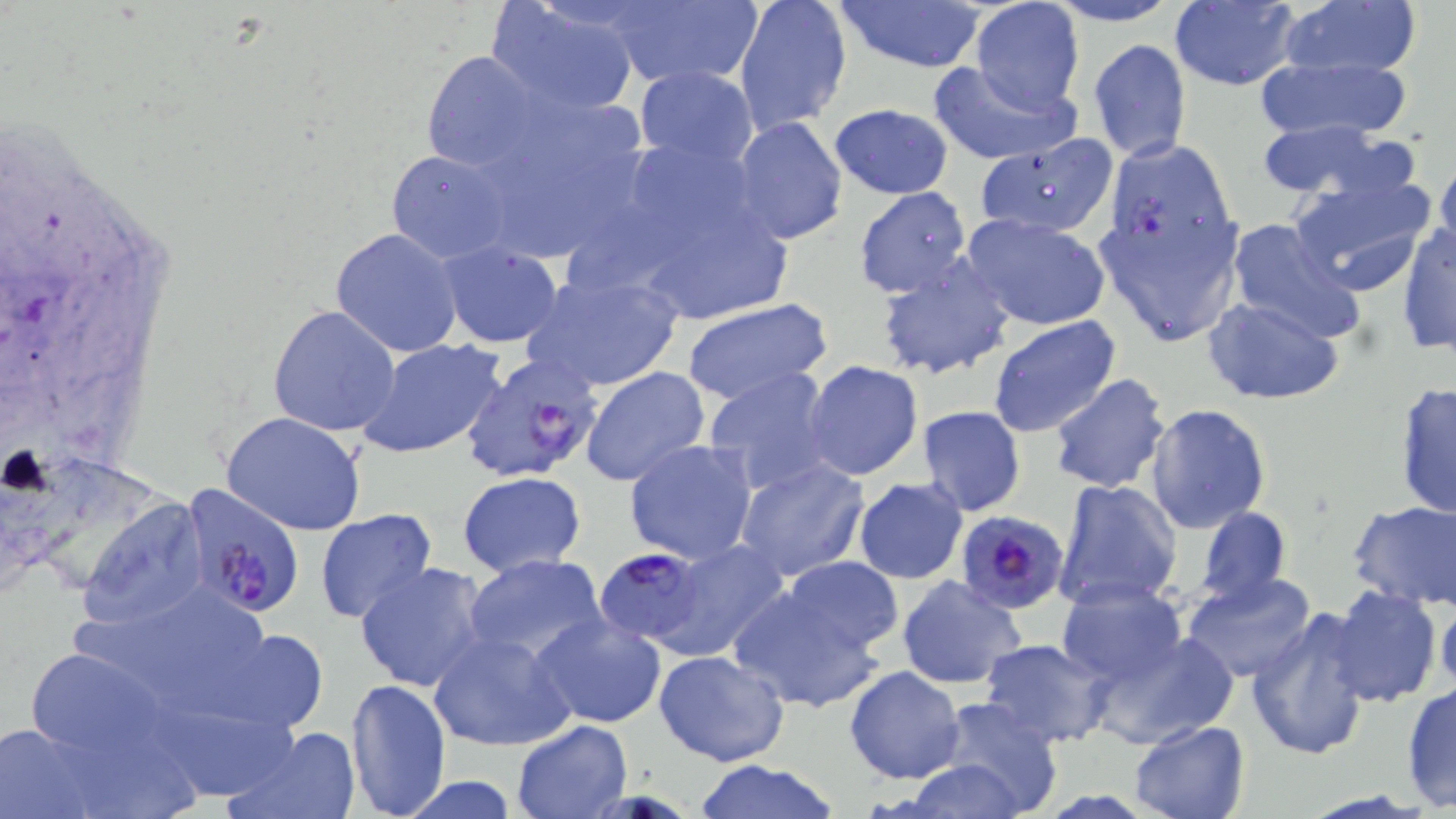
slide-level diagnosis = Plasmodium falciparum
modality = light microscopy
image size = 1456×819 pixels
magnification = 1000x
stain = May-Grünwald-Giemsa
Plasmodium falciparum-infected red blood cell locations = approximate bounding boxes as (x1,y1)-(x2,y2) corner pairs in pixels: (461,354)-(602,482), (183,488)-(307,616), (955,510)-(1069,614), (596,547)-(707,646)
uninfected red blood cell locations = approximate bounding boxes as (x1,y1)-(x2,y2) corner pairs in pixels: (734,0)-(852,135), (832,0)-(990,74), (1043,0)-(1183,26), (1168,0)-(1299,90), (1272,0)-(1425,87), (488,1)-(640,115), (970,2)-(1087,115), (597,3)-(760,89), (1089,39)-(1191,164), (420,49)-(545,174), (1254,52)-(1412,142), (926,60)-(1079,164), (634,64)-(759,165), (828,103)-(955,200), (732,116)-(847,244), (1254,118)-(1405,202), (979,136)-(1117,242), (386,149)-(516,264), (1092,154)-(1246,347), (1433,155)-(1456,263), (1286,169)-(1438,298), (624,175)-(802,324), (852,186)-(972,298), (960,212)-(1113,331), (1222,218)-(1366,344), (1397,222)-(1456,356), (330,227)-(464,359), (436,245)-(561,348), (875,254)-(1015,381), (517,268)-(685,395), (1202,295)-(1345,405), (680,297)-(834,405), (267,304)-(402,436), (987,315)-(1123,440), (358,339)-(506,459), (804,360)-(923,482), (580,366)-(709,488), (704,367)-(838,495), (1048,374)-(1171,493), (1393,381)-(1456,522), (1145,404)-(1273,535), (917,407)-(1027,516), (221,413)-(367,536), (624,439)-(758,565), (736,457)-(870,583), (457,471)-(586,577), (852,478)-(968,585), (1052,479)-(1181,611), (79,498)-(209,631), (1348,500)-(1456,610), (1195,506)-(1290,607), (313,508)-(439,625), (654,537)-(791,664), (463,555)-(609,668), (778,556)-(905,654), (355,562)-(492,692), (1178,571)-(1321,684), (896,575)-(1027,689), (63,580)-(269,680), (1056,580)-(1187,685), (728,582)-(889,713), (1324,585)-(1443,708), (1435,589)-(1456,698), (1244,607)-(1373,763), (532,614)-(669,729), (174,629)-(326,736), (1083,629)-(1237,751), (426,630)-(577,752), (977,638)-(1113,747), (23,645)-(173,765), (653,650)-(790,767), (845,665)-(965,784), (343,677)-(452,817), (1401,683)-(1455,813), (929,696)-(1066,817), (153,702)-(315,792), (42,719)-(204,819), (510,719)-(632,819), (1129,720)-(1249,819), (0,722)-(109,818), (231,725)-(361,819), (899,758)-(1035,819), (693,761)-(843,819)
field of view = one of a larger specimen
preparation = thin blood film